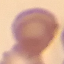 Malaria status: uninfected. Giemsa stain. Thin blood film. Acquired by smartphone through the microscope eyepiece. Automatically extracted cell patch, resized to 64 × 64 pixels.